Report the malaria status of this cell.
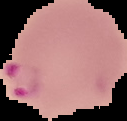
Parasitized.

{
  "image_type": "segmented cell region on a black background",
  "image_size": "127×121 pixels",
  "preparation": "thin blood film"
}